Describe the morphology of the red blood cells.
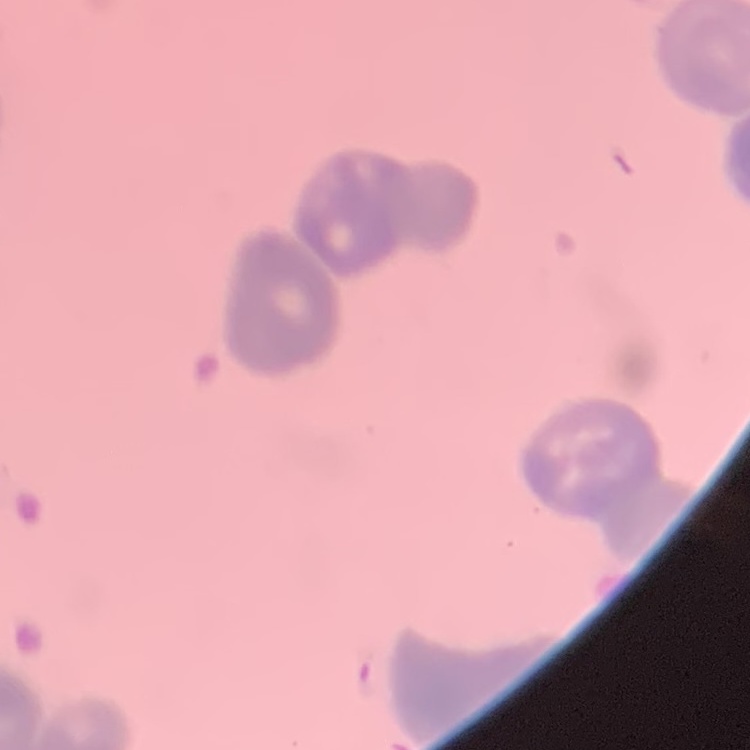
They show rouleaux formation.

image type = one tile cut from a larger photomicrograph
preparation = thin peripheral smear
stain = Field's or Giemsa